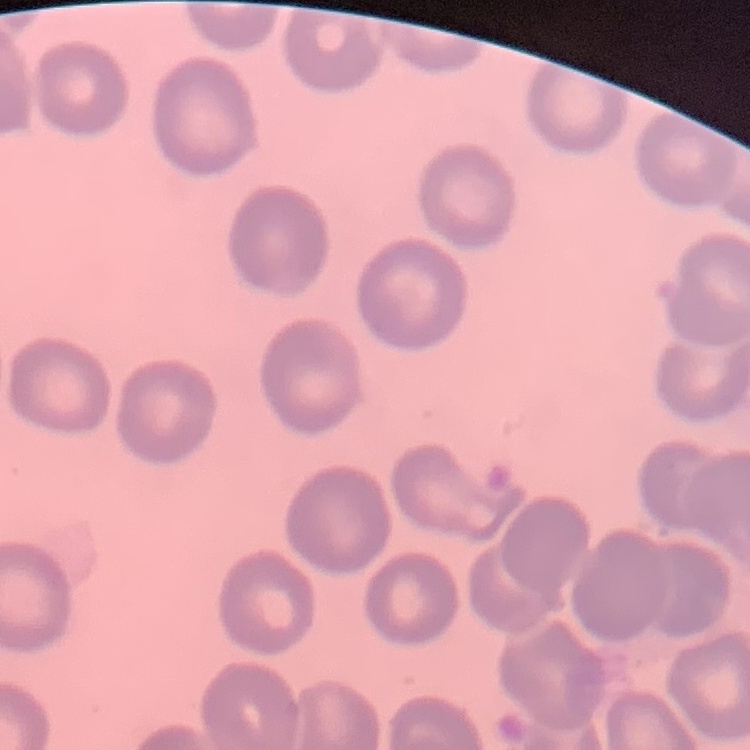

The erythrocytes show no rouleaux formation. Thin blood smear. Square crop of a larger photomicrograph. Stained with either Field's or Giemsa.